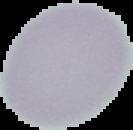 From a thin blood film. Malaria status: uninfected. Cell region segmented out of the field of view; the surrounding area is masked to black. Image is 133×130 pixels.